Locate every blood parasite and identify its species.
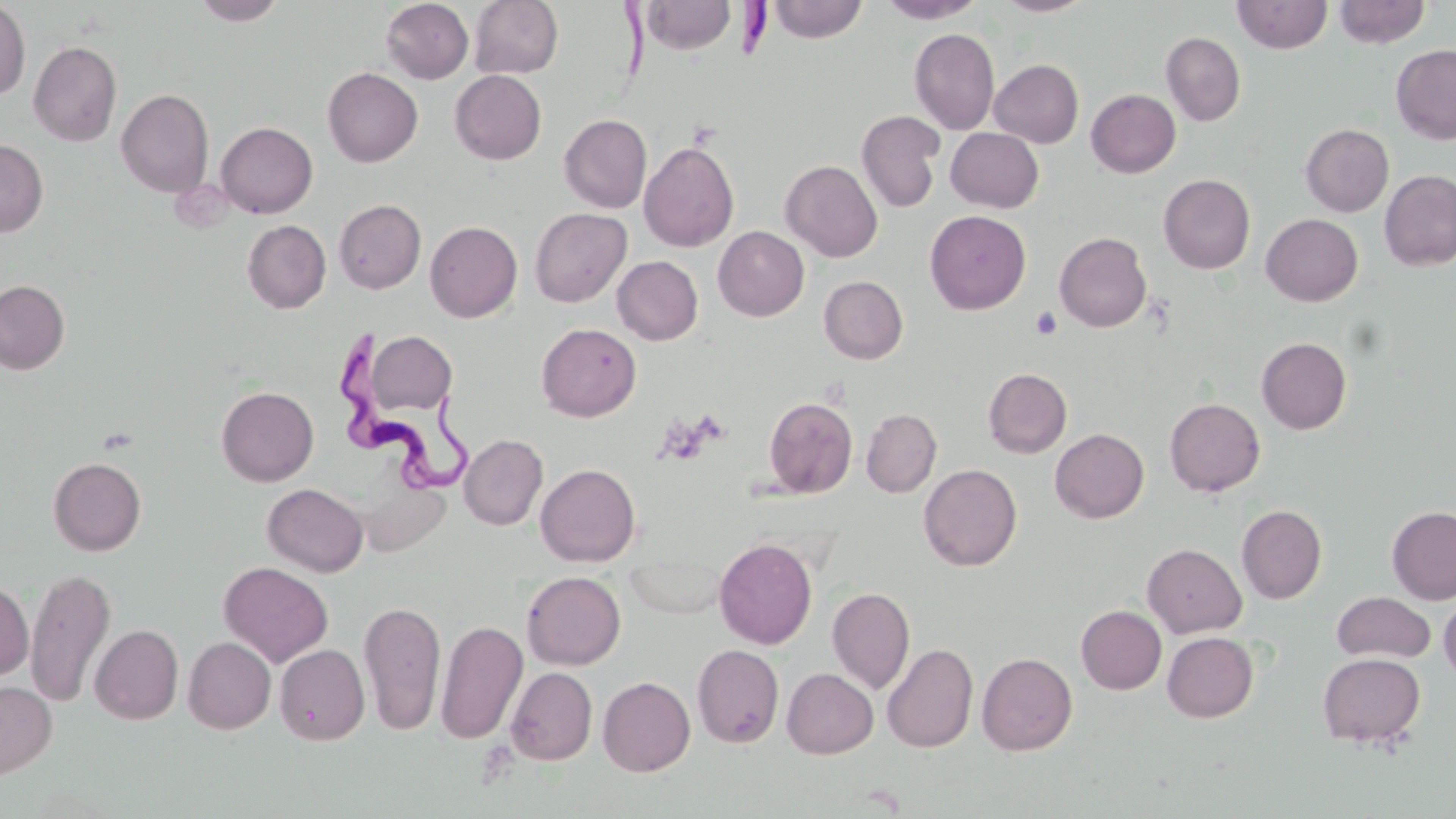
Approximate bounding boxes as (x1, y1, x2, y2) in pixels.
Trypanosoma brucei: (613, 0, 771, 84), (339, 330, 479, 499).
No Plasmodium falciparum, Plasmodium ovale, Plasmodium malariae, Plasmodium vivax, or Babesia divergens observed.

Summary:
  - Uninfected red blood cell locations: (192, 0, 288, 25), (381, 0, 474, 84), (469, 0, 564, 79), (767, 0, 868, 43), (877, 0, 986, 23), (993, 0, 1095, 17), (1232, 0, 1332, 54), (1333, 0, 1430, 48), (639, 1, 736, 55), (0, 2, 31, 100), (909, 28, 1000, 134), (1161, 32, 1246, 126), (28, 40, 122, 146), (1391, 44, 1456, 145), (989, 59, 1084, 147), (322, 67, 423, 167), (450, 70, 546, 164), (116, 88, 214, 198), (1086, 89, 1181, 178), (857, 110, 946, 213), (559, 114, 652, 213), (215, 121, 318, 218), (1300, 124, 1394, 216), (945, 127, 1044, 212), (0, 139, 48, 237), (639, 141, 739, 252), (781, 160, 882, 262), (1379, 170, 1456, 271), (1158, 174, 1255, 274), (334, 199, 426, 294), (529, 208, 632, 307), (925, 210, 1032, 314), (1261, 214, 1363, 306), (242, 220, 331, 314), (425, 221, 522, 322), (713, 226, 809, 321), (1054, 232, 1152, 333), (612, 256, 703, 345), (819, 276, 908, 363), (0, 280, 70, 374), (536, 323, 641, 421), (364, 331, 457, 415), (1256, 337, 1352, 434), (983, 368, 1072, 459), (216, 386, 319, 486), (763, 397, 858, 499), (1164, 397, 1265, 497), (861, 408, 942, 497), (1050, 428, 1149, 523), (459, 434, 548, 530), (47, 456, 146, 556), (535, 463, 641, 567), (919, 464, 1022, 571), (262, 483, 368, 576), (1236, 505, 1327, 604), (1387, 506, 1456, 604), (714, 537, 817, 650), (1142, 543, 1247, 638), (625, 552, 729, 619), (218, 561, 334, 667), (25, 567, 116, 708), (522, 571, 625, 670), (0, 579, 34, 681), (827, 586, 915, 694), (1331, 591, 1436, 663), (1439, 592, 1456, 685), (359, 599, 446, 736), (1076, 605, 1166, 694), (436, 619, 528, 745), (90, 624, 183, 724), (1162, 632, 1258, 722), (183, 637, 276, 733), (692, 643, 785, 748), (882, 643, 978, 753), (275, 644, 369, 746), (977, 651, 1077, 755), (1317, 652, 1425, 748), (505, 666, 598, 765), (782, 668, 878, 758), (598, 676, 695, 776), (0, 680, 57, 778)
  - Platelet locations: (1030, 306, 1062, 340)
  - Slide-level diagnosis: Trypanosoma brucei
  - Magnification: 1000x
  - Preparation: thin blood smear
  - Image size: 1456×819 pixels
  - Modality: optical microscopy
  - Field of view: single
  - Stain: May-Grünwald-Giemsa